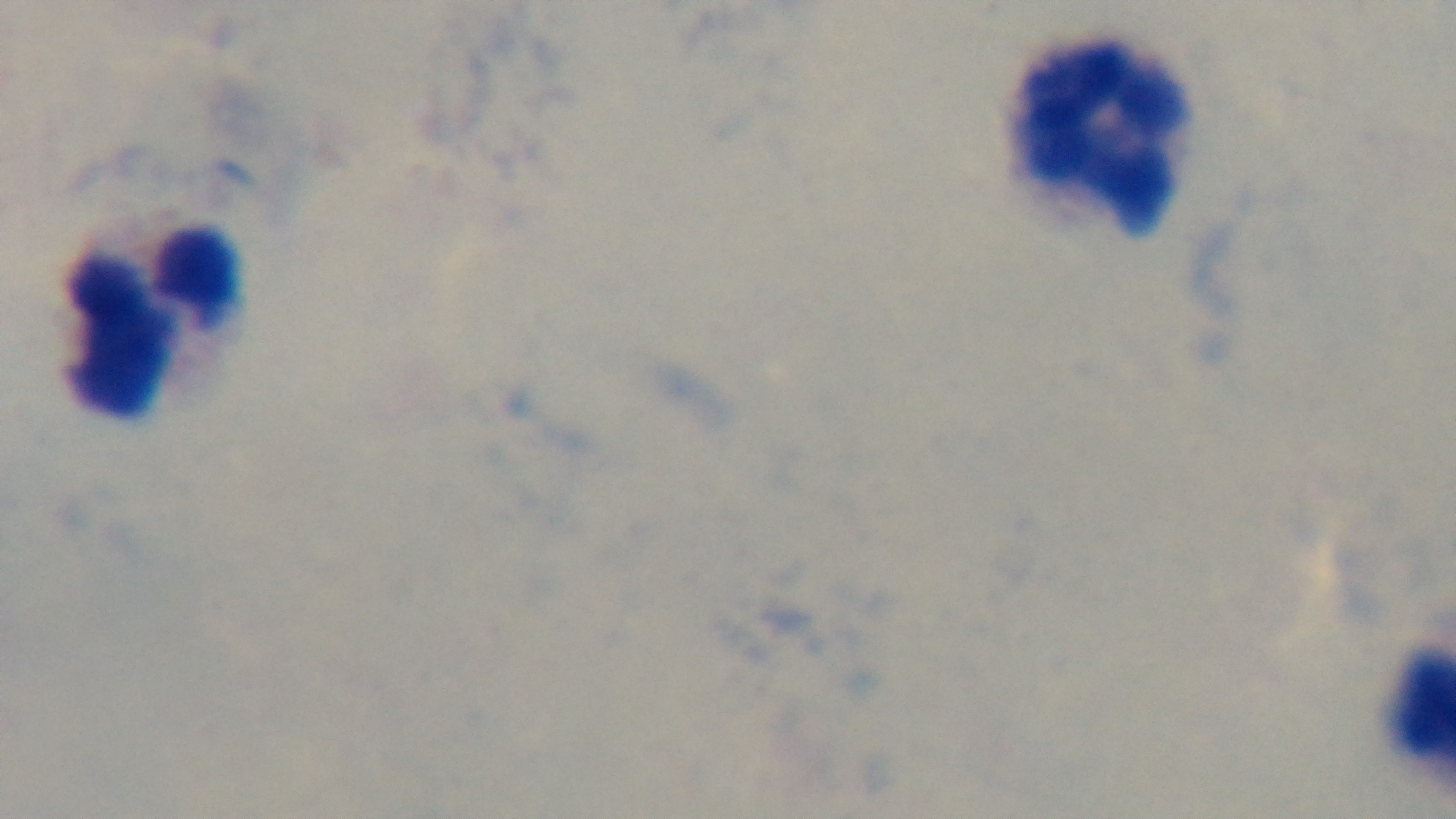

field_of_view: single
capture: mounted 4K digital camera
stain: Giemsa
modality: light microscopy
objective: 100x oil immersion
preparation: thick smear
malaria_status: uninfected